Report the malaria status of this cell.
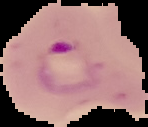
It is parasitized.

From a thin blood smear. Image is 148×127 pixels. The area outside the segmented cell region is set to black.